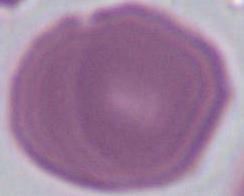

Summary:
  - Identification: red blood cell
  - Modality: photomicrograph
  - Magnification: 1000x